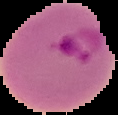

preparation = thin blood film
image type = segmented cell region on a black background
image size = 118×115 pixels
malaria status = parasitized